Report the malaria status of this cell.
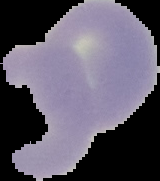
It is uninfected.

Summary:
  - Image size: 160×181 pixels
  - Preparation: thin blood smear
  - Image type: segmented cell region on a black background